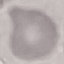
Malaria status: uninfected. Cell patch, automatically extracted from a larger field of view and resized to 64 × 64 pixels. Acquired by smartphone through the microscope eyepiece. Giemsa stain. Thin blood smear.